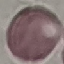

Summary:
  - Malaria status: uninfected
  - Capture: smartphone camera at the microscope eyepiece
  - Stain: Giemsa
  - Image type: cell patch, automatically extracted from a larger field of view and resized to 64 × 64 pixels
  - Preparation: thin blood film